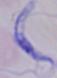
magnification: 1000x
modality: photomicrograph
identification: trypanosome